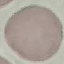 Result: no malaria parasites detected. Acquired by smartphone through the microscope eyepiece. Thin blood smear. Giemsa stain. Automatically extracted cell patch, resized to 64 × 64 pixels.